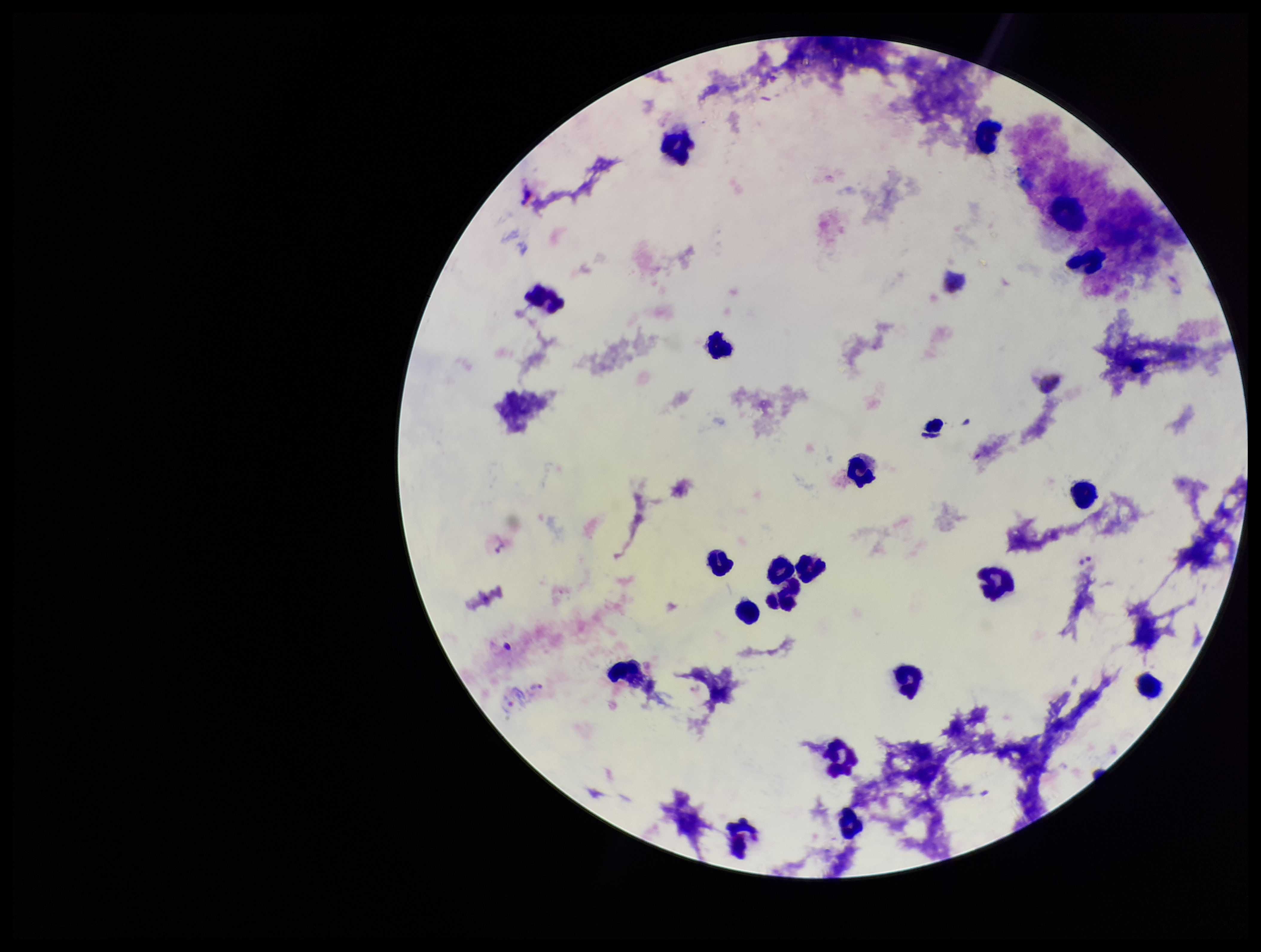

Summary:
  - Parasite count: 0
  - Preparation: thick
  - Patient malaria status: positive
  - Leukocyte count: 20
  - Image size: 1261×952 pixels
  - Plasmodium parasites: none seen
  - Stain: Giemsa
  - Capture: smartphone photograph through the microscope eyepiece
  - Field of view: single
  - Species reported for this patient: Plasmodium vivax